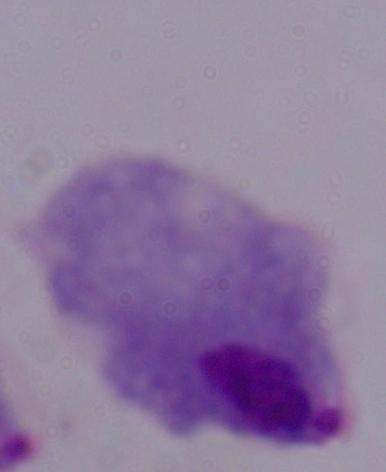
A trichomonad is seen. Captured at 1000x magnification. Micrograph.